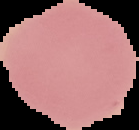

Summary:
  - Image size: 139×130 pixels
  - Preparation: thin blood film
  - Image type: segmented cell region on a black background
  - Result: no malaria parasites detected